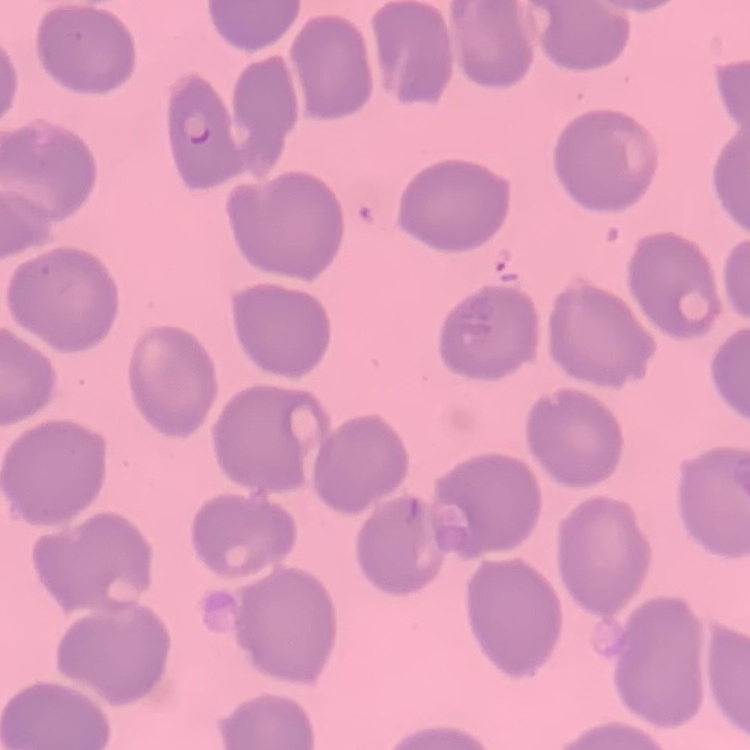
The red blood cells show no rouleaux formation. Stained with either Field's or Giemsa. One tile cut from a larger photomicrograph. Thin blood film.